State the blood parasite species.
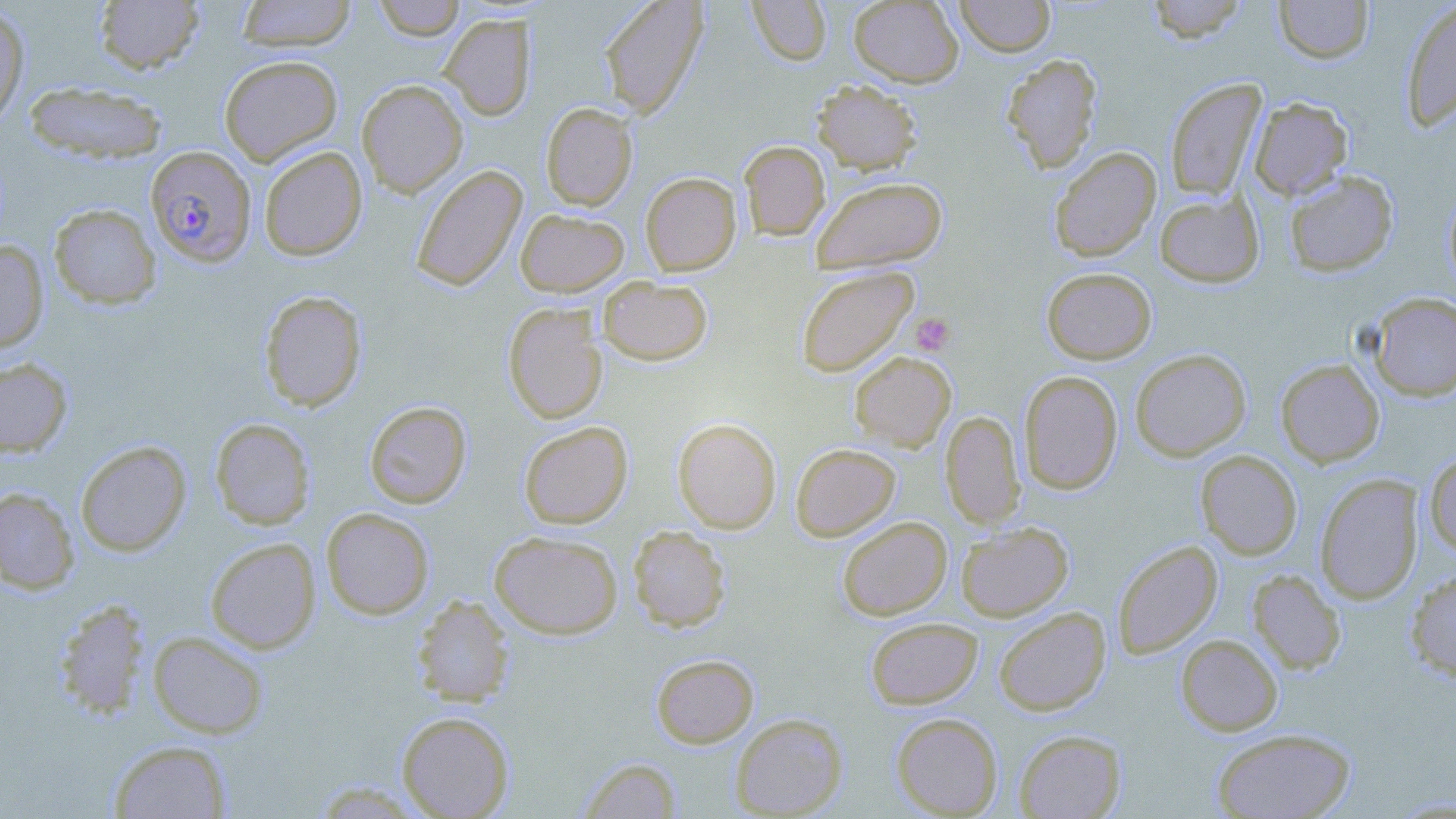
Plasmodium falciparum.

Approximate bounding boxes as [x1, y1, x2, y2] in pixels. Uninfected red blood cell locations: [94, 0, 205, 75], [236, 0, 357, 51], [373, 0, 465, 40], [599, 0, 708, 118], [848, 0, 964, 87], [955, 0, 1055, 57], [1144, 0, 1250, 43], [1274, 0, 1374, 64], [746, 1, 833, 66], [1400, 1, 1456, 132], [0, 4, 30, 128], [439, 14, 536, 120], [1002, 53, 1102, 173], [219, 54, 343, 166], [1165, 78, 1267, 200], [356, 79, 468, 197], [812, 79, 923, 175], [23, 81, 168, 163], [1249, 97, 1352, 200], [540, 103, 638, 210], [739, 141, 830, 240], [259, 146, 367, 261], [1049, 147, 1161, 261], [410, 164, 527, 292], [1284, 170, 1399, 277], [640, 172, 741, 276], [811, 176, 947, 274], [1443, 185, 1456, 293], [1154, 190, 1265, 288], [49, 203, 161, 310], [516, 208, 629, 296], [0, 240, 49, 352], [795, 266, 918, 377], [1041, 267, 1156, 364], [598, 276, 713, 366], [259, 290, 367, 412], [1369, 292, 1456, 401], [502, 303, 608, 424], [1130, 348, 1251, 462], [849, 352, 956, 452], [0, 358, 73, 456], [1275, 359, 1385, 468], [1019, 370, 1123, 494], [364, 401, 472, 508], [940, 411, 1025, 529], [210, 418, 316, 530], [672, 418, 781, 533], [518, 421, 633, 529], [75, 440, 191, 556], [790, 443, 901, 541], [1196, 450, 1303, 560], [1425, 453, 1456, 557], [1315, 473, 1423, 604], [0, 487, 79, 595], [321, 507, 435, 620], [837, 516, 952, 621], [956, 522, 1073, 621], [628, 526, 731, 632], [489, 530, 624, 639], [205, 537, 321, 653], [1112, 540, 1223, 659], [1406, 568, 1456, 682], [1248, 569, 1346, 674], [412, 594, 514, 707], [53, 599, 153, 721], [993, 606, 1111, 716], [865, 617, 983, 709], [148, 631, 268, 738], [1175, 634, 1283, 736], [651, 653, 759, 747], [397, 711, 514, 819], [891, 712, 1003, 817], [730, 713, 848, 818], [1212, 727, 1356, 818], [1014, 730, 1126, 819], [108, 740, 233, 818], [577, 757, 683, 818]. Platelet locations: [909, 312, 955, 356]. Plasmodium falciparum-infected red blood cell locations: [145, 145, 257, 267]. Image is 1456×819 pixels. May-Grünwald-Giemsa-stained preparation. Thin blood film. Captured at 1000x magnification. Single field of view. Optical microscopy.